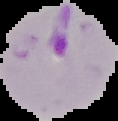
preparation = thin blood film
image type = cell region segmented out of the field of view; surrounding area masked to black
image size = 118×121 pixels
result = malaria parasites detected